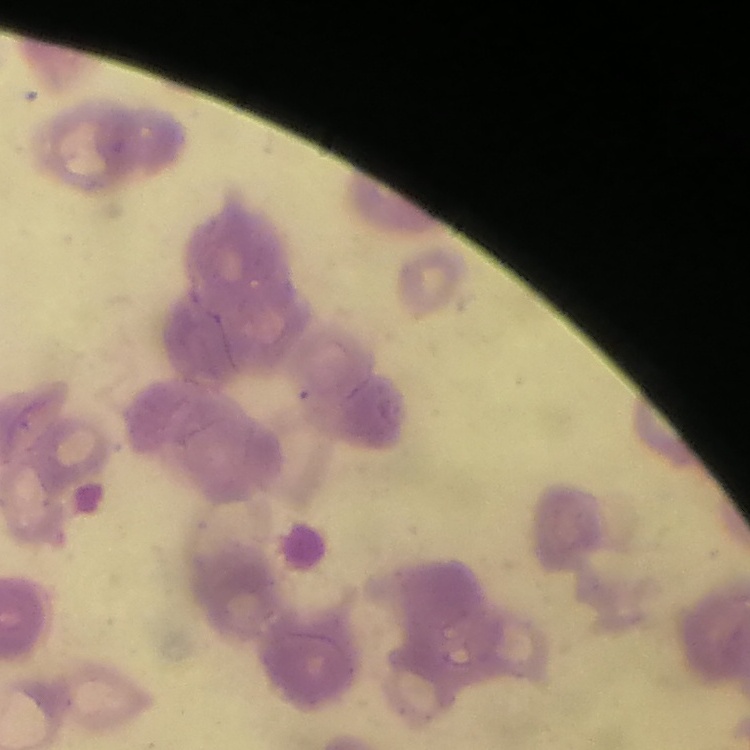

Summary:
  - Erythrocyte morphology: rouleaux formation
  - Stain: Field's or Giemsa
  - Image type: square crop of a larger photomicrograph
  - Preparation: thin blood smear